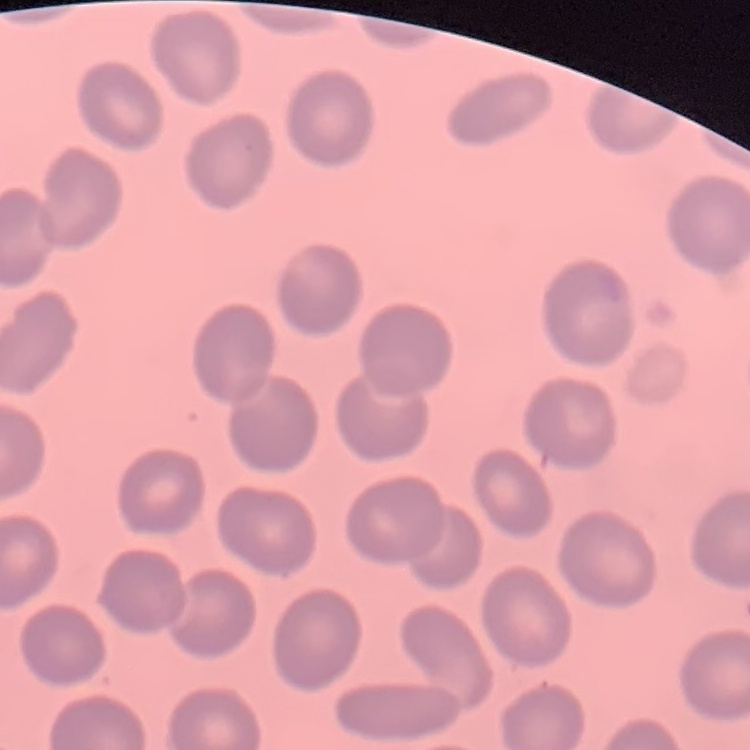

red blood cell morphology = no rouleaux formation
image type = one tile cut from a larger photomicrograph
preparation = thin blood film
stain = Field's or Giemsa